Name the parasite shown.
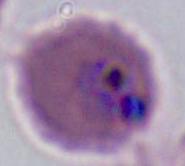

Plasmodium.

Summary:
  - Modality: micrograph
  - Magnification: 400x or 1000x